Locate every leukocyte (white blood cell).
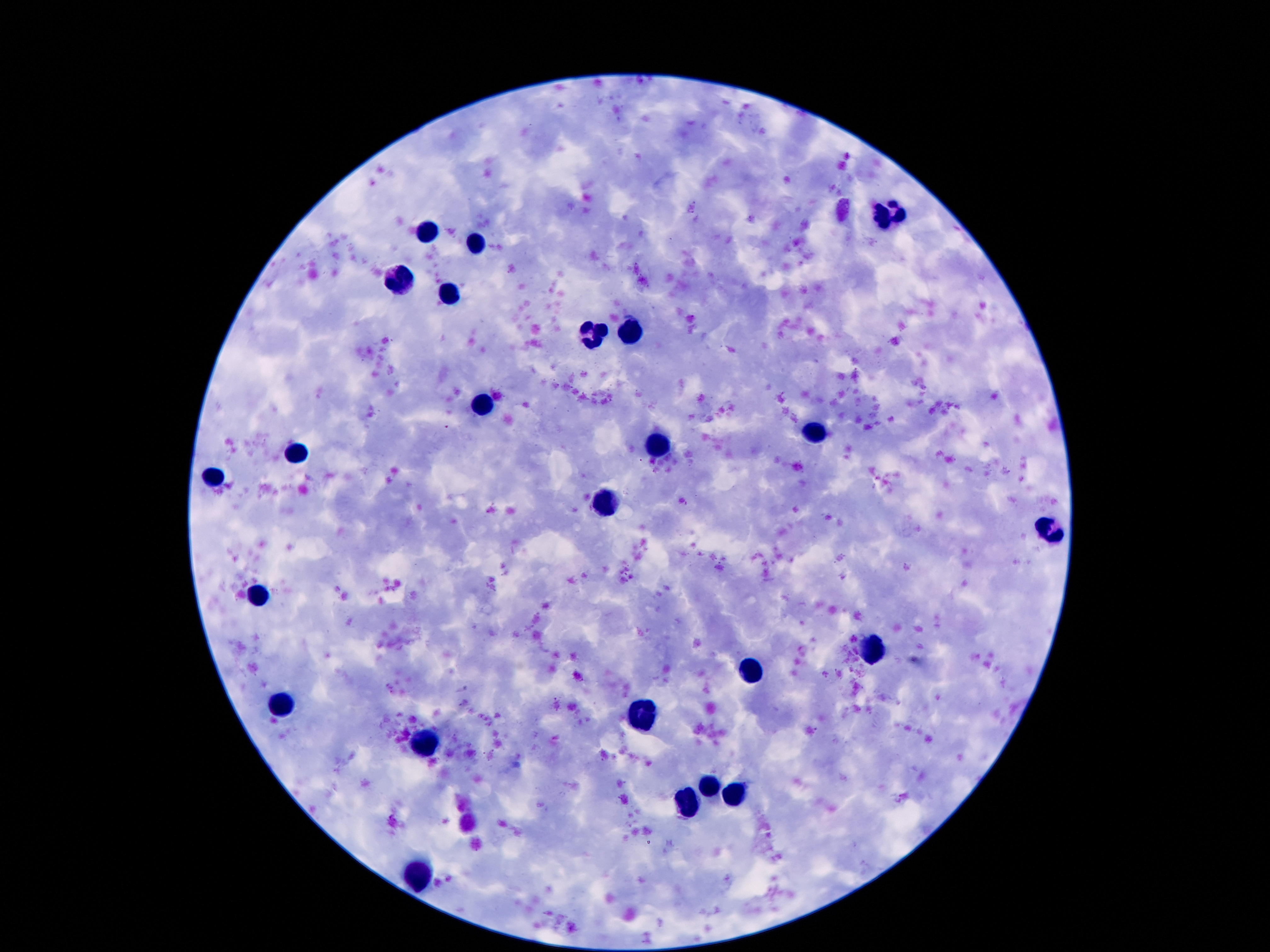

Approximate centers as (x, y) in pixels.
Leukocytes: (892, 211), (425, 232), (475, 243), (400, 281), (450, 293), (631, 333), (593, 338), (483, 406), (811, 433), (658, 447), (297, 452), (214, 473), (606, 506), (1047, 531), (261, 593), (876, 650), (752, 670), (286, 704), (642, 713), (427, 743), (711, 786), (734, 797), (688, 802), (420, 873).

Summary:
  - Stain: Giemsa
  - Magnification: 100x
  - Preparation: thick blood smear
  - Image size: 1270×952 pixels
  - Patient malaria status: uninfected
  - Field of view: one from this slide
  - Capture: smartphone camera through the microscope eyepiece